Identify the parasite.
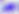

This is Toxoplasma gondii.

{
  "modality": "micrograph",
  "magnification": "400x"
}